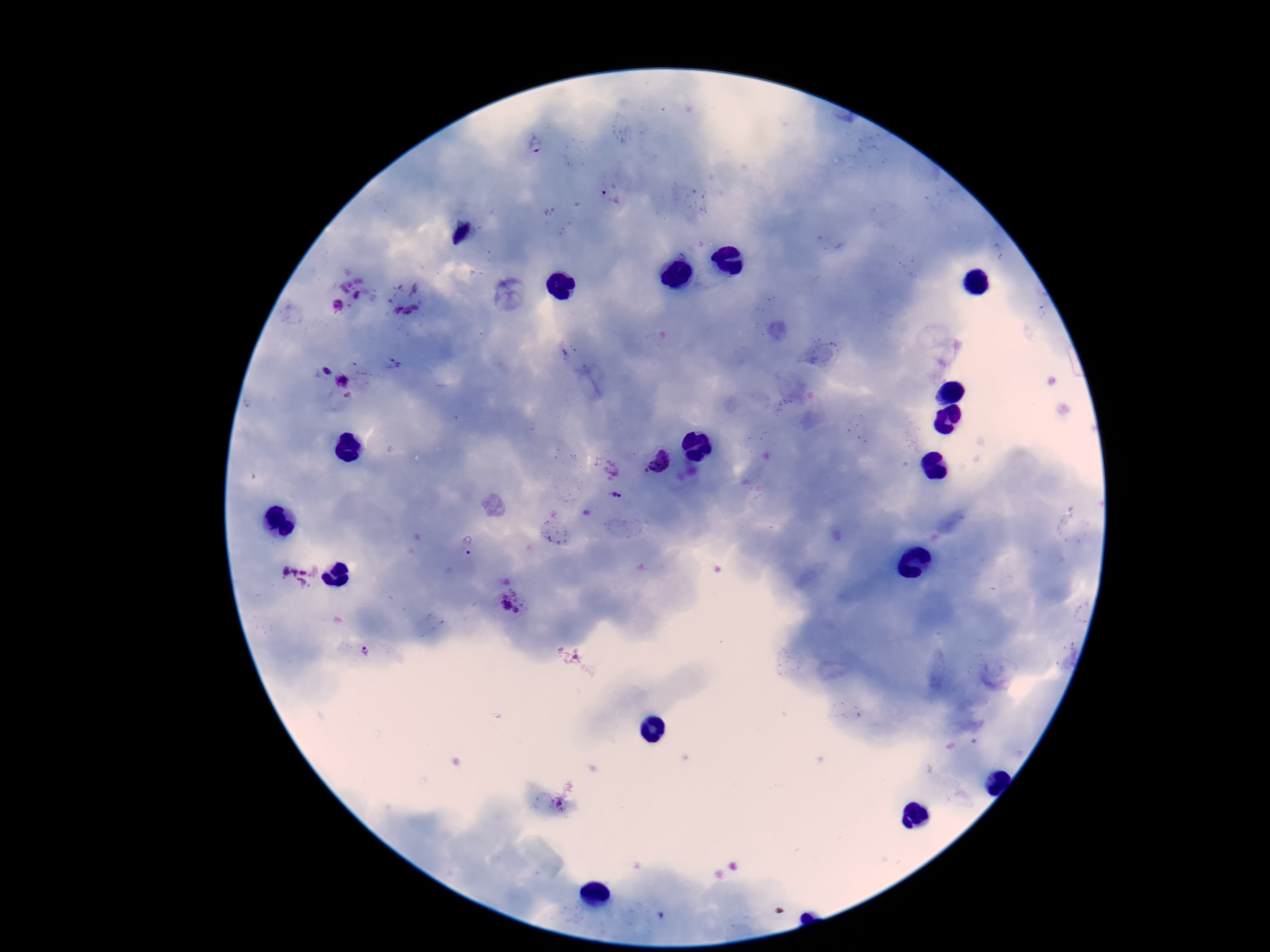

field of view = single
patient malaria status = positive
preparation = thick blood smear
image size = 1270×952 pixels
magnification = 100x
capture = smartphone camera through the microscope eyepiece
Plasmodium parasite locations = approximate centers as {x, y} in pixels: {536, 147}, {611, 196}, {357, 297}, {338, 306}, {397, 309}, {412, 310}, {327, 373}, {343, 381}, {660, 462}, {614, 494}, {620, 496}, {469, 545}, {285, 571}, {304, 571}, {295, 572}, {303, 582}, {506, 597}, {516, 597}, {506, 605}, {516, 610}, {366, 651}
stain = Giemsa